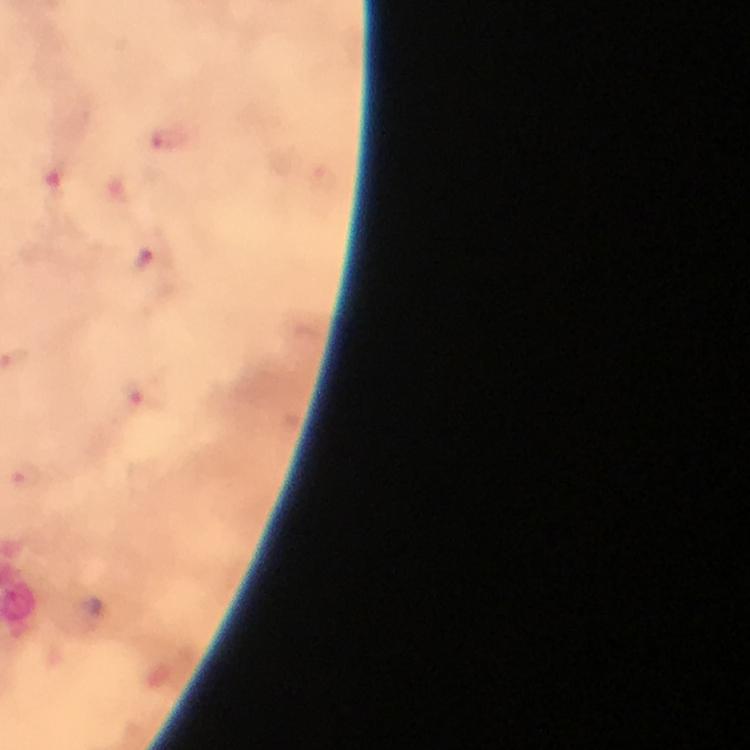

capture = smartphone photograph through a microscope
context = from a malaria diagnostic workup
immersion oil = used
stain = Giemsa
preparation = thick smear
cropped from = one field of view
image size = 750×750 pixels
Plasmodium parasite locations = approximate centers as [x, y] in pixels: [170, 140], [145, 263], [134, 397], [26, 475]
magnification = 100x